Outline each Plasmodium vivax-infected red blood cell.
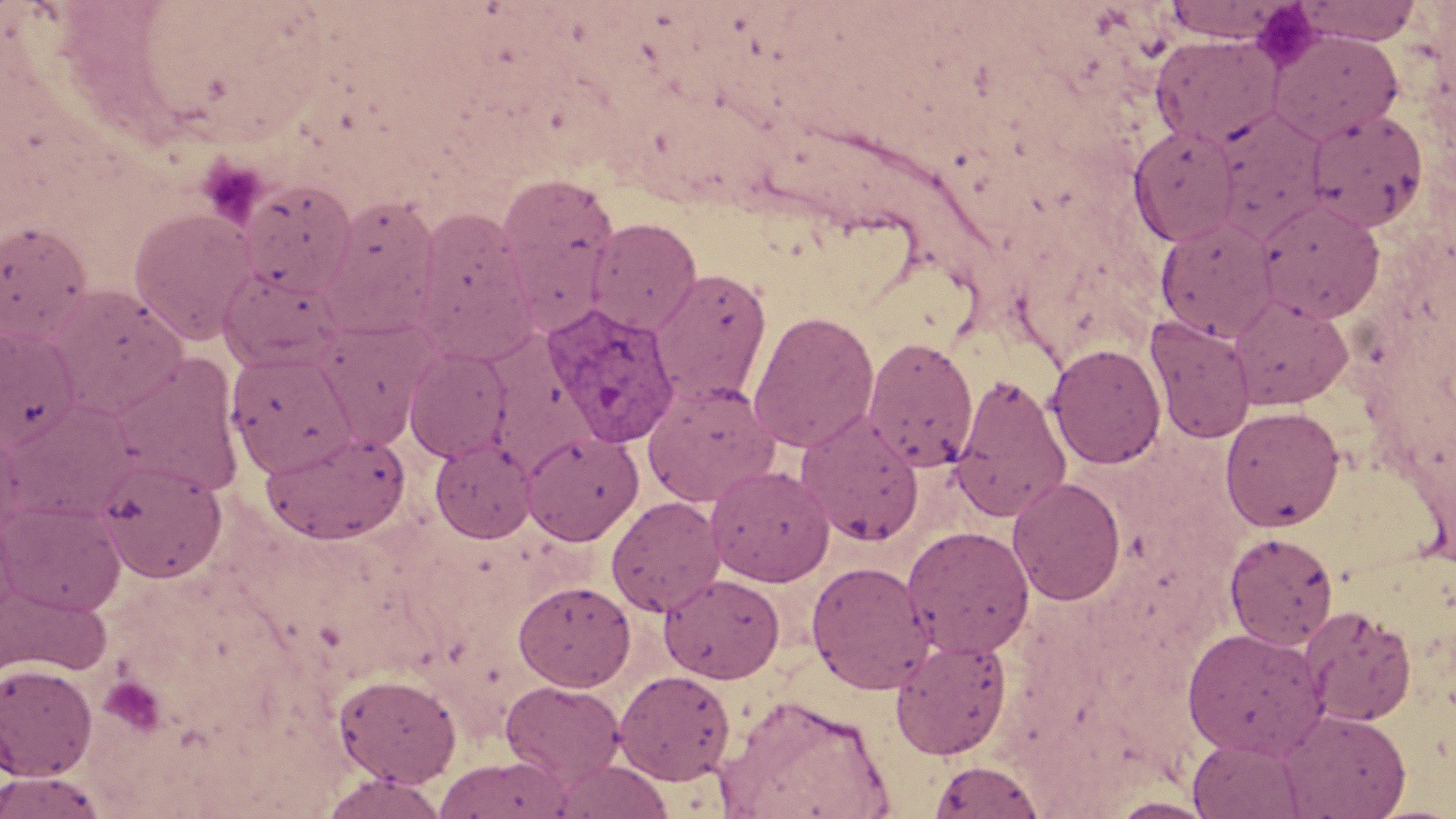
Approximate bounding boxes as [x1, y1, x2, y2] in pixels.
Plasmodium vivax-infected red blood cells: [545, 304, 680, 448].

Platelet locations: [1250, 2, 1322, 69], [98, 676, 167, 737]. Uninfected red blood cell locations: [1162, 0, 1288, 42], [1298, 0, 1421, 45], [1269, 29, 1403, 143], [1151, 35, 1282, 148], [1211, 109, 1327, 240], [1304, 109, 1428, 233], [1129, 125, 1240, 247], [496, 172, 620, 319], [239, 180, 357, 296], [322, 193, 441, 326], [1257, 197, 1385, 322], [129, 207, 257, 343], [412, 207, 533, 349], [587, 217, 702, 335], [1156, 217, 1279, 342], [0, 220, 93, 344], [220, 264, 346, 372], [651, 267, 772, 405], [47, 285, 188, 417], [1228, 294, 1353, 410], [748, 309, 880, 453], [1145, 316, 1256, 445], [0, 326, 80, 449], [863, 336, 979, 471], [1046, 343, 1166, 469], [403, 347, 513, 463], [226, 351, 356, 477], [111, 354, 245, 497], [951, 374, 1071, 522], [642, 380, 780, 506], [3, 400, 138, 520], [1219, 405, 1345, 531], [796, 412, 924, 546], [0, 428, 31, 541], [262, 429, 411, 544], [522, 431, 644, 545], [431, 440, 535, 543], [95, 458, 227, 583], [706, 464, 835, 587], [1008, 477, 1126, 605], [606, 496, 725, 616], [0, 501, 126, 616], [902, 525, 1035, 658], [1223, 532, 1339, 650], [806, 560, 935, 694], [659, 573, 785, 683], [513, 580, 636, 691], [0, 582, 111, 678], [1301, 606, 1416, 726], [1182, 626, 1328, 760], [891, 636, 1013, 759], [0, 662, 98, 780], [614, 669, 736, 785], [335, 673, 461, 787], [501, 680, 626, 785], [720, 694, 894, 819], [1278, 709, 1411, 818], [1187, 737, 1306, 818], [435, 754, 570, 819], [549, 759, 675, 819], [928, 759, 1046, 819], [1, 770, 108, 818], [320, 771, 448, 818], [1103, 796, 1219, 818]. Slide-level diagnosis: Plasmodium vivax. Captured at 1000x magnification. Thin blood film. One field of a larger specimen. Optical microscopy. Image is 1456×819 pixels. May-Grünwald-Giemsa stain.